Name the parasite shown.
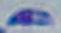

This is Toxoplasma gondii.

1000x magnification. Photomicrograph.